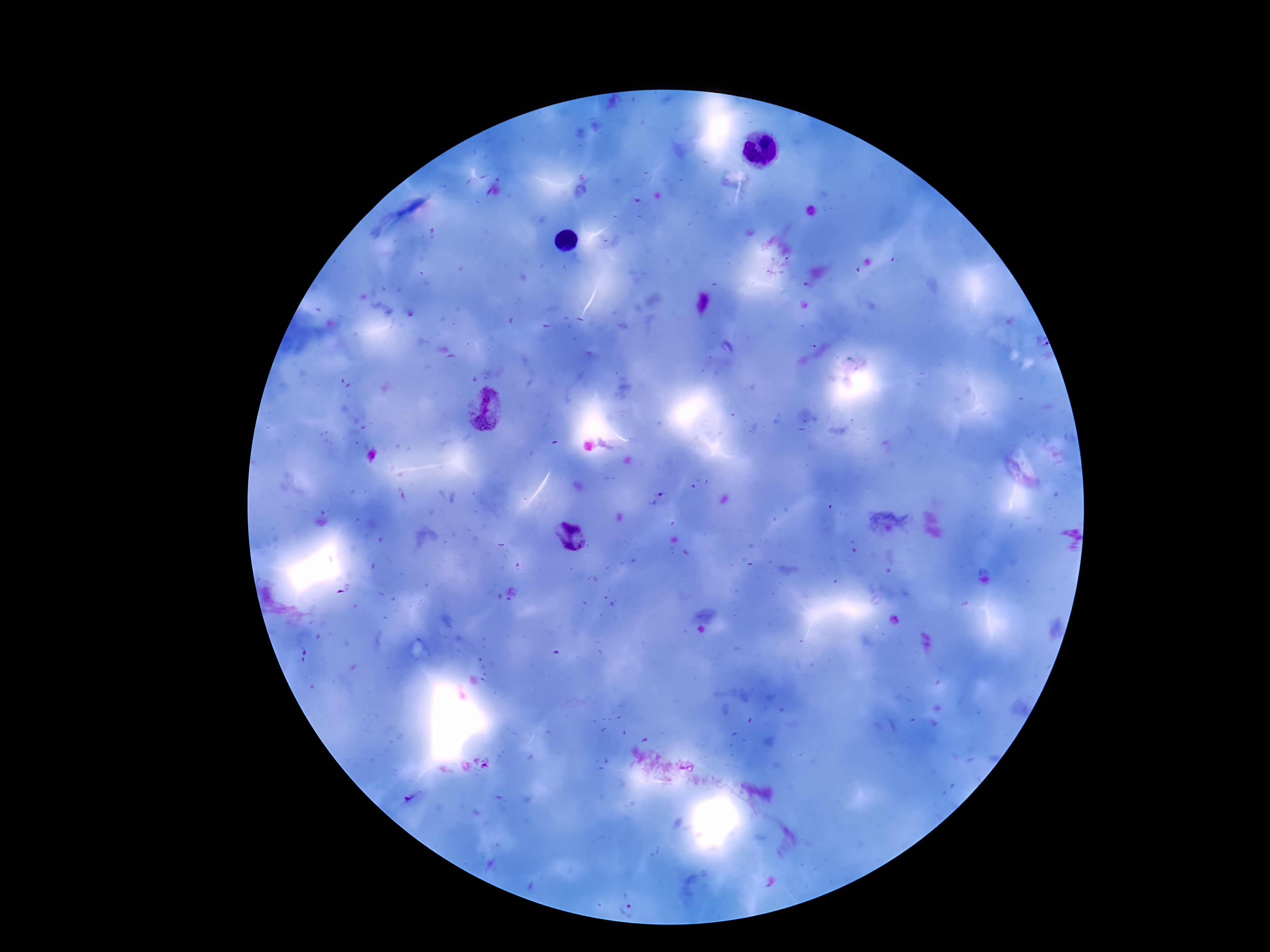
Approximate object centers, in pixels from the top-left corner.
Summary:
  - Plasmodium parasite locations: (x=488, y=409), (x=661, y=500), (x=567, y=535), (x=413, y=798), (x=629, y=905)
  - Preparation: thick blood smear
  - Image size: 1270×952 pixels
  - Field of view: single
  - Magnification: 100x
  - Patient malaria status: positive
  - Capture: smartphone camera through the microscope eyepiece
  - Stain: Giemsa